State which parasite is depicted.
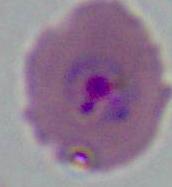
This is Plasmodium.

modality: photomicrograph
magnification: 400x or 1000x